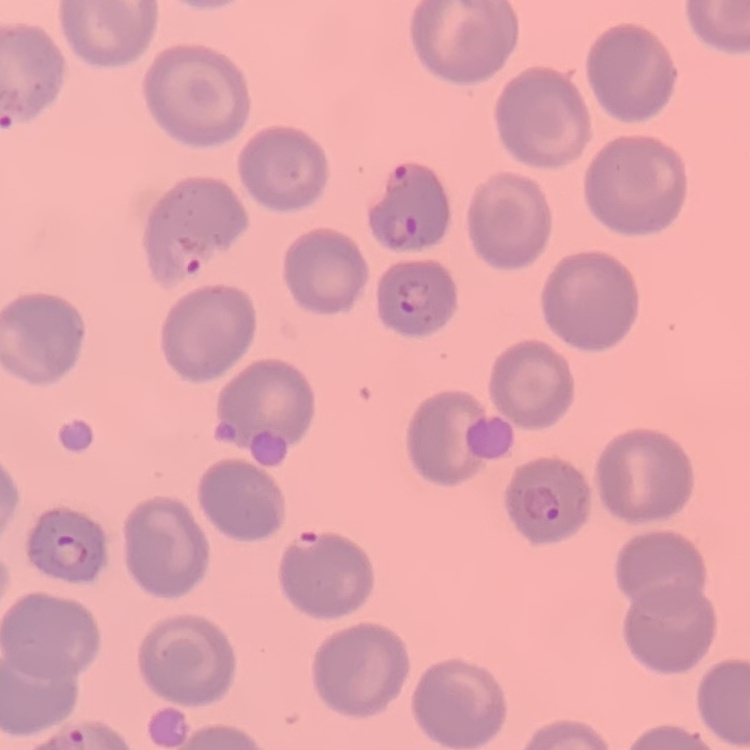 The erythrocytes show no rouleaux formation. Square crop of a larger photomicrograph. Thin blood smear. Field's or Giemsa stain.